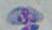

{
  "identification": "Toxoplasma gondii",
  "modality": "micrograph",
  "magnification": "1000x"
}